Outline each Trypanosoma brucei.
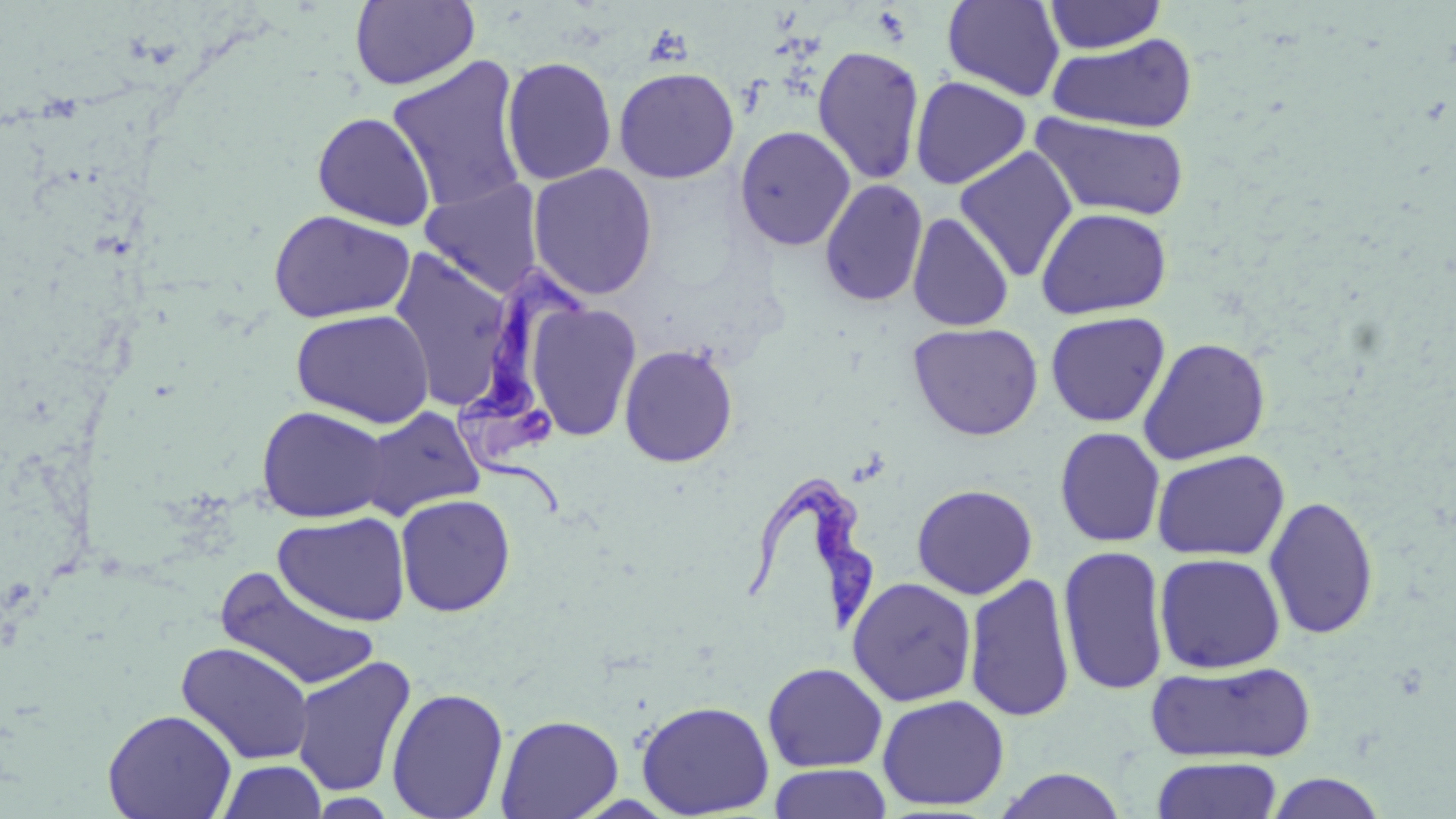

Approximate bounding boxes as (x1, y1, x2, y2) in pixels.
Trypanosoma brucei: (453, 261, 587, 519), (746, 472, 876, 632).

Uninfected red blood cell locations: (942, 0, 1065, 102), (1042, 0, 1167, 54), (350, 1, 479, 90), (1046, 33, 1199, 134), (812, 45, 925, 185), (386, 56, 528, 215), (501, 57, 618, 186), (613, 66, 739, 183), (910, 76, 1031, 189), (312, 112, 435, 231), (1031, 113, 1192, 221), (734, 125, 856, 251), (954, 146, 1078, 283), (528, 163, 658, 300), (419, 178, 544, 298), (819, 179, 928, 307), (1036, 206, 1173, 319), (268, 210, 415, 323), (907, 212, 1014, 332), (388, 249, 515, 411), (527, 302, 642, 441), (290, 309, 435, 428), (1045, 311, 1170, 427), (907, 321, 1043, 441), (1138, 336, 1272, 465), (619, 343, 738, 467), (256, 405, 392, 523), (358, 406, 485, 520), (1054, 427, 1165, 547), (1152, 449, 1289, 561), (911, 483, 1038, 599), (395, 494, 516, 617), (1263, 495, 1379, 641), (274, 511, 411, 626), (1057, 545, 1170, 696), (1154, 552, 1286, 674), (215, 568, 381, 692), (964, 573, 1076, 724), (846, 577, 977, 707), (176, 641, 315, 765), (290, 656, 416, 797), (1144, 660, 1317, 764), (762, 662, 888, 772), (386, 686, 508, 819), (876, 694, 1010, 811), (636, 700, 775, 818), (102, 708, 237, 819), (496, 713, 623, 819), (1151, 756, 1283, 819), (216, 760, 328, 819), (769, 763, 892, 819), (993, 769, 1128, 819), (1263, 771, 1389, 818). Slide-level diagnosis: Trypanosoma brucei. Captured at 1000x magnification. Light microscopy. Thin blood smear. Image is 1456×819 pixels. May-Grünwald-Giemsa-stained preparation. Single field of view.